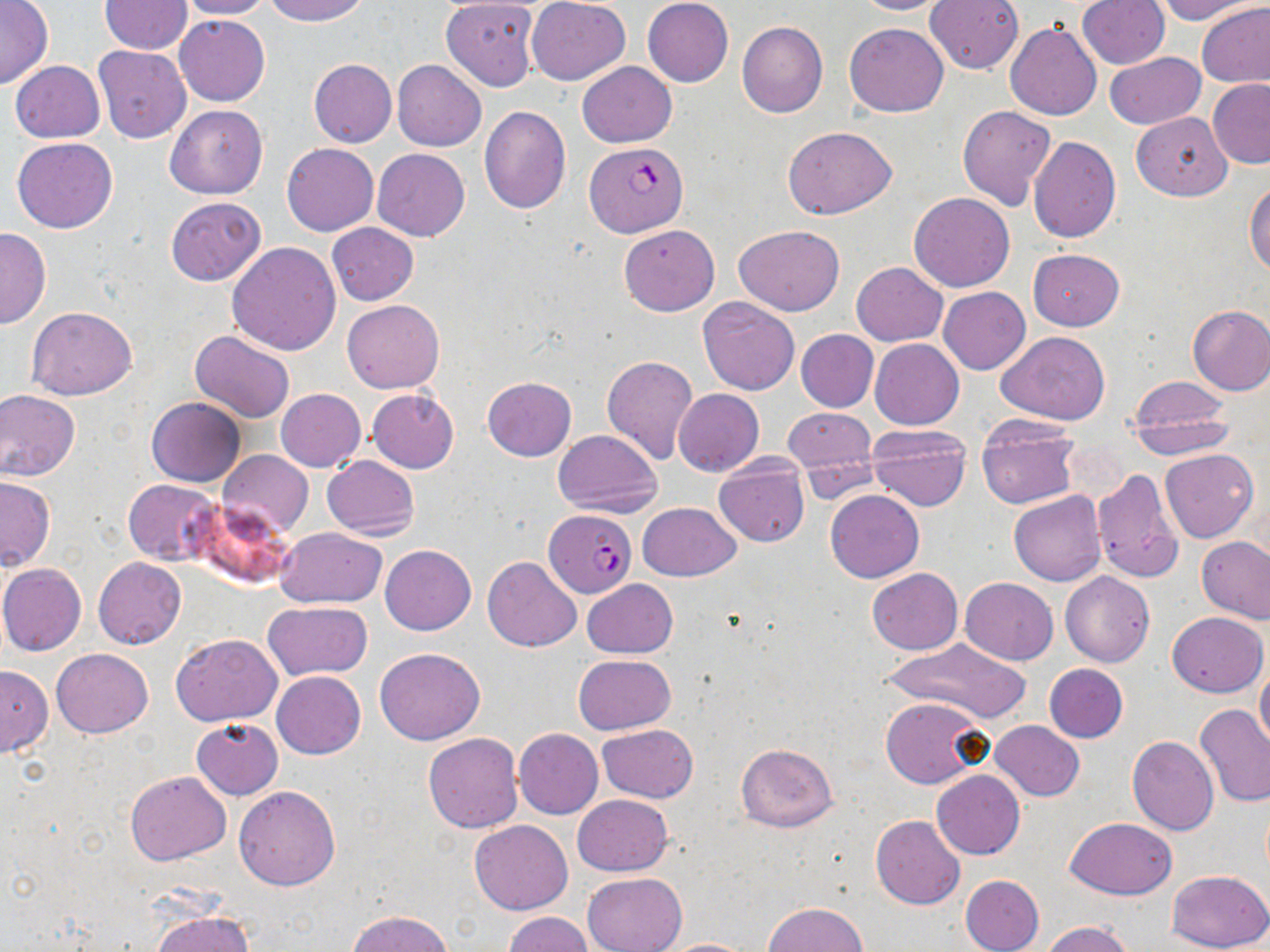

slide-level diagnosis = Plasmodium falciparum
preparation = thin blood film
modality = light microscopy
field of view = single
uninfected red blood cell locations = approximate bounding boxes as named x1/y1/x2/y2 corners in pixels: (x1=100, y1=0, x2=192, y2=54), (x1=177, y1=0, x2=277, y2=20), (x1=263, y1=0, x2=367, y2=25), (x1=527, y1=0, x2=630, y2=84), (x1=642, y1=0, x2=733, y2=87), (x1=851, y1=0, x2=951, y2=16), (x1=926, y1=0, x2=1024, y2=74), (x1=1152, y1=0, x2=1259, y2=23), (x1=0, y1=1, x2=53, y2=89), (x1=442, y1=1, x2=539, y2=91), (x1=1078, y1=1, x2=1169, y2=69), (x1=1198, y1=2, x2=1270, y2=88), (x1=175, y1=15, x2=270, y2=105), (x1=736, y1=20, x2=828, y2=117), (x1=844, y1=21, x2=949, y2=117), (x1=1005, y1=22, x2=1102, y2=121), (x1=93, y1=45, x2=190, y2=142), (x1=1103, y1=52, x2=1205, y2=130), (x1=308, y1=59, x2=397, y2=147), (x1=11, y1=60, x2=106, y2=142), (x1=392, y1=60, x2=486, y2=152), (x1=577, y1=61, x2=676, y2=147), (x1=1207, y1=79, x2=1270, y2=168), (x1=164, y1=104, x2=267, y2=199), (x1=479, y1=106, x2=570, y2=214), (x1=957, y1=106, x2=1056, y2=210), (x1=1131, y1=112, x2=1233, y2=199), (x1=783, y1=125, x2=896, y2=220), (x1=1028, y1=135, x2=1121, y2=242), (x1=12, y1=138, x2=118, y2=233), (x1=282, y1=144, x2=378, y2=235), (x1=373, y1=149, x2=470, y2=241), (x1=1244, y1=180, x2=1270, y2=277), (x1=909, y1=193, x2=1016, y2=292), (x1=166, y1=197, x2=266, y2=285), (x1=327, y1=223, x2=418, y2=305), (x1=619, y1=224, x2=719, y2=316), (x1=734, y1=225, x2=845, y2=316), (x1=0, y1=227, x2=50, y2=329), (x1=226, y1=241, x2=340, y2=355), (x1=1028, y1=248, x2=1124, y2=330), (x1=851, y1=262, x2=948, y2=346), (x1=939, y1=286, x2=1030, y2=374), (x1=697, y1=296, x2=802, y2=395), (x1=341, y1=299, x2=445, y2=392), (x1=1186, y1=304, x2=1270, y2=394), (x1=27, y1=306, x2=136, y2=400), (x1=189, y1=330, x2=297, y2=423), (x1=796, y1=330, x2=878, y2=412), (x1=997, y1=331, x2=1111, y2=423), (x1=870, y1=339, x2=965, y2=431), (x1=601, y1=356, x2=698, y2=465), (x1=1125, y1=375, x2=1236, y2=452), (x1=482, y1=377, x2=576, y2=460), (x1=275, y1=388, x2=365, y2=472), (x1=368, y1=388, x2=459, y2=473), (x1=0, y1=389, x2=80, y2=481), (x1=674, y1=389, x2=763, y2=475), (x1=146, y1=396, x2=244, y2=486), (x1=784, y1=407, x2=875, y2=484), (x1=1130, y1=415, x2=1235, y2=458), (x1=976, y1=416, x2=1080, y2=510), (x1=866, y1=425, x2=969, y2=511), (x1=553, y1=429, x2=662, y2=517), (x1=1161, y1=449, x2=1258, y2=543), (x1=217, y1=450, x2=313, y2=538), (x1=322, y1=454, x2=419, y2=541), (x1=712, y1=457, x2=809, y2=548), (x1=1091, y1=467, x2=1185, y2=585), (x1=0, y1=476, x2=56, y2=570), (x1=123, y1=479, x2=223, y2=565), (x1=826, y1=489, x2=924, y2=582), (x1=1008, y1=490, x2=1106, y2=585), (x1=190, y1=499, x2=294, y2=588), (x1=637, y1=503, x2=741, y2=581), (x1=275, y1=527, x2=386, y2=608), (x1=1196, y1=536, x2=1269, y2=624), (x1=381, y1=545, x2=476, y2=636), (x1=483, y1=556, x2=582, y2=652), (x1=93, y1=557, x2=186, y2=648), (x1=0, y1=563, x2=87, y2=656), (x1=867, y1=568, x2=962, y2=655), (x1=1060, y1=571, x2=1154, y2=666), (x1=961, y1=578, x2=1059, y2=664), (x1=583, y1=579, x2=677, y2=658), (x1=263, y1=601, x2=373, y2=681), (x1=1167, y1=612, x2=1267, y2=697), (x1=171, y1=632, x2=283, y2=725), (x1=883, y1=638, x2=1033, y2=721), (x1=52, y1=648, x2=153, y2=738), (x1=374, y1=648, x2=485, y2=745), (x1=572, y1=654, x2=676, y2=735), (x1=1044, y1=663, x2=1128, y2=743), (x1=0, y1=665, x2=52, y2=757), (x1=1255, y1=665, x2=1270, y2=752), (x1=271, y1=670, x2=365, y2=759), (x1=881, y1=697, x2=985, y2=788), (x1=1196, y1=704, x2=1270, y2=807), (x1=191, y1=719, x2=284, y2=800), (x1=990, y1=720, x2=1083, y2=801), (x1=597, y1=723, x2=698, y2=802), (x1=514, y1=729, x2=603, y2=819), (x1=423, y1=732, x2=522, y2=833), (x1=1127, y1=737, x2=1219, y2=836), (x1=736, y1=743, x2=837, y2=832), (x1=932, y1=770, x2=1025, y2=859), (x1=125, y1=772, x2=231, y2=866), (x1=234, y1=785, x2=340, y2=891), (x1=572, y1=795, x2=674, y2=876), (x1=870, y1=815, x2=965, y2=910), (x1=1066, y1=818, x2=1178, y2=899), (x1=469, y1=819, x2=572, y2=915), (x1=1166, y1=869, x2=1270, y2=952), (x1=582, y1=872, x2=687, y2=952), (x1=961, y1=874, x2=1045, y2=952), (x1=765, y1=902, x2=867, y2=952), (x1=346, y1=909, x2=454, y2=952), (x1=151, y1=911, x2=254, y2=952), (x1=502, y1=912, x2=593, y2=952), (x1=1040, y1=921, x2=1136, y2=952), (x1=660, y1=938, x2=756, y2=952)
image size = 1270×952 pixels
magnification = 1000x
Plasmodium falciparum-infected red blood cell locations = approximate bounding boxes as named x1/y1/x2/y2 corners in pixels: (x1=585, y1=141, x2=689, y2=239), (x1=544, y1=508, x2=636, y2=597)
stain = May-Grünwald-Giemsa